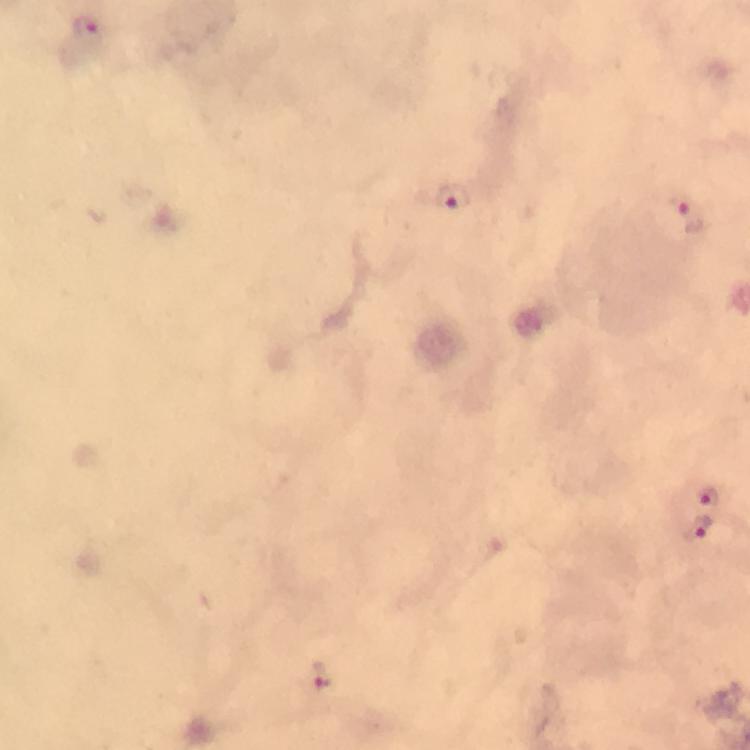
Approximate object centers, in pixels from the top-left corner.
Summary:
  - Malaria parasite locations: (x=87, y=29), (x=453, y=199), (x=688, y=218), (x=707, y=493), (x=697, y=529), (x=320, y=673)
  - Cropped from: one field of view
  - Magnification: 100x
  - Context: from a malaria diagnostic workup
  - Preparation: thick blood film
  - Stain: Giemsa
  - Immersion oil: applied
  - Image size: 750×750 pixels
  - Capture: smartphone camera through the microscope